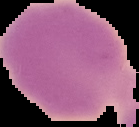

preparation = thin blood film
image size = 139×127 pixels
image type = segmented cell region on a black background
malaria status = uninfected